Classify this cell by malaria status.
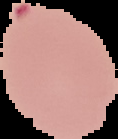

It is parasitized.

image_type: cell region segmented out of the field of view; surrounding area masked to black
preparation: thin blood film
image_size: 118×139 pixels